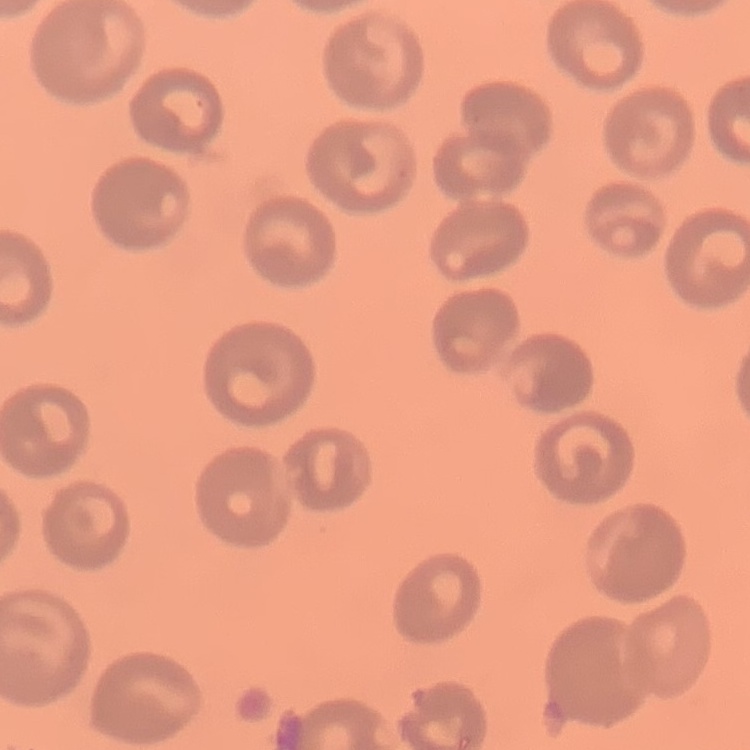
red_blood_cell_morphology: no rouleaux formation
preparation: thin blood smear
stain: Field's or Giemsa
image_type: square crop of a larger photomicrograph